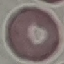

{
  "malaria_status": "uninfected",
  "image_type": "cell patch, automatically extracted from a larger field of view and resized to 64 × 64 pixels",
  "preparation": "thin blood film",
  "capture": "smartphone through the microscope eyepiece",
  "stain": "Giemsa"
}